Assess this cell for malaria.
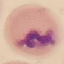
It is uninfected.

Photographed with a smartphone camera at the microscope eyepiece. Giemsa-stained preparation. Thin blood smear. Cell patch, automatically extracted from a larger field of view and resized to 64 × 64 pixels.